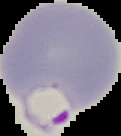

Summary:
  - Preparation: thin blood smear
  - Result: Plasmodium parasites identified
  - Image type: segmented cell region with the area outside set to black
  - Image size: 121×136 pixels